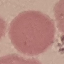

result = no malaria parasites detected
preparation = thin blood film
image type = automatically extracted cell patch, resized to 64 × 64 pixels
stain = Giemsa
capture = smartphone camera at the microscope eyepiece